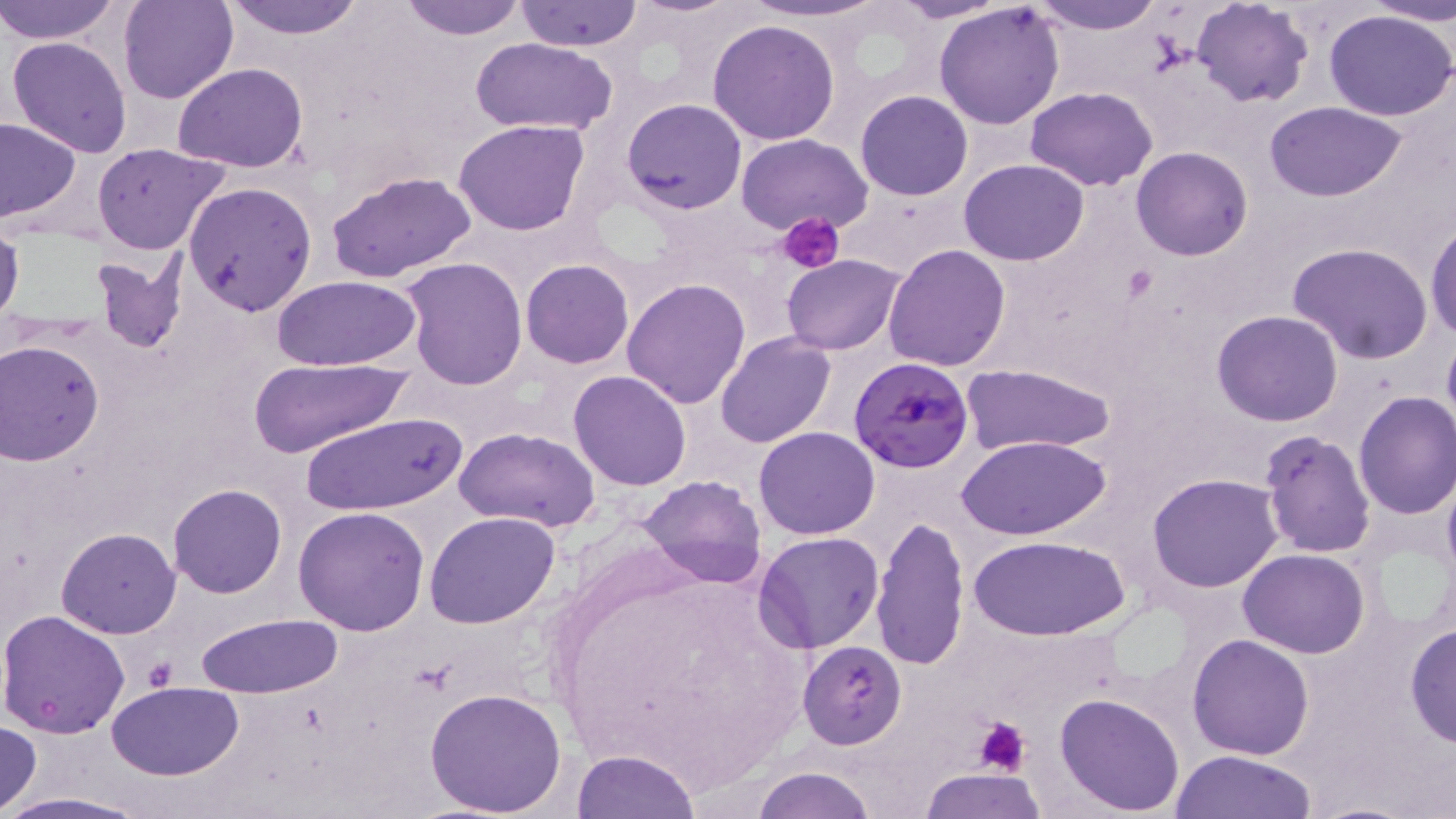

Summary:
  - Coordinate format: approximate bounding boxes as [x1, y1, x2, y2] in pixels
  - Uninfected red blood cell locations: [0, 0, 123, 45], [116, 0, 237, 105], [220, 0, 368, 39], [738, 0, 891, 24], [888, 0, 1014, 23], [1030, 0, 1165, 34], [1191, 0, 1314, 107], [1369, 0, 1456, 27], [394, 1, 533, 40], [515, 1, 643, 50], [829, 1, 944, 110], [934, 2, 1065, 131], [1324, 9, 1456, 122], [706, 19, 840, 145], [6, 36, 132, 158], [470, 37, 618, 134], [173, 63, 308, 172], [1025, 86, 1157, 191], [855, 90, 972, 201], [622, 98, 747, 215], [1265, 102, 1407, 200], [0, 118, 81, 222], [453, 119, 592, 236], [735, 133, 875, 239], [91, 142, 230, 255], [1131, 146, 1253, 261], [959, 159, 1089, 266], [325, 170, 477, 283], [182, 181, 318, 317], [1426, 219, 1456, 342], [0, 221, 25, 333], [1287, 242, 1434, 364], [882, 243, 1012, 371], [87, 254, 187, 355], [781, 254, 907, 356], [401, 259, 527, 389], [521, 259, 635, 369], [270, 276, 421, 371], [621, 278, 752, 409], [1211, 310, 1344, 428], [1441, 328, 1456, 440], [714, 331, 836, 447], [1, 339, 107, 467], [250, 357, 411, 456], [961, 363, 1116, 454], [568, 371, 692, 491], [1353, 389, 1456, 519], [300, 412, 466, 516], [754, 426, 880, 539], [455, 427, 600, 531], [1259, 430, 1376, 559], [959, 434, 1110, 540], [1148, 474, 1283, 592], [639, 476, 766, 588], [168, 483, 287, 598], [293, 506, 429, 633], [425, 510, 560, 630], [873, 513, 970, 671], [57, 527, 182, 639], [754, 531, 885, 652], [971, 533, 1128, 641], [1237, 549, 1369, 658], [0, 610, 132, 738], [193, 614, 344, 699], [1405, 623, 1456, 748], [1187, 633, 1314, 759], [799, 642, 906, 748], [106, 682, 245, 780], [425, 688, 567, 815], [1055, 691, 1186, 814], [0, 720, 41, 813], [572, 749, 699, 819], [1168, 750, 1319, 818], [749, 766, 875, 819], [921, 768, 1047, 819], [0, 792, 156, 818]
  - Plasmodium falciparum-infected red blood cell locations: [848, 355, 977, 474]
  - Platelet locations: [779, 214, 846, 273], [142, 658, 175, 688], [974, 716, 1028, 777]
  - Slide-level diagnosis: Plasmodium falciparum
  - Field of view: one of a larger specimen
  - Preparation: thin blood film
  - Magnification: 1000x
  - Image size: 1456×819 pixels
  - Stain: May-Grünwald-Giemsa
  - Modality: light microscopy